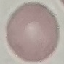
result = no malaria parasites seen
image type = cell patch, automatically extracted from a larger field of view and resized to 64 × 64 pixels
preparation = thin blood smear
capture = smartphone through the microscope eyepiece
stain = Giemsa